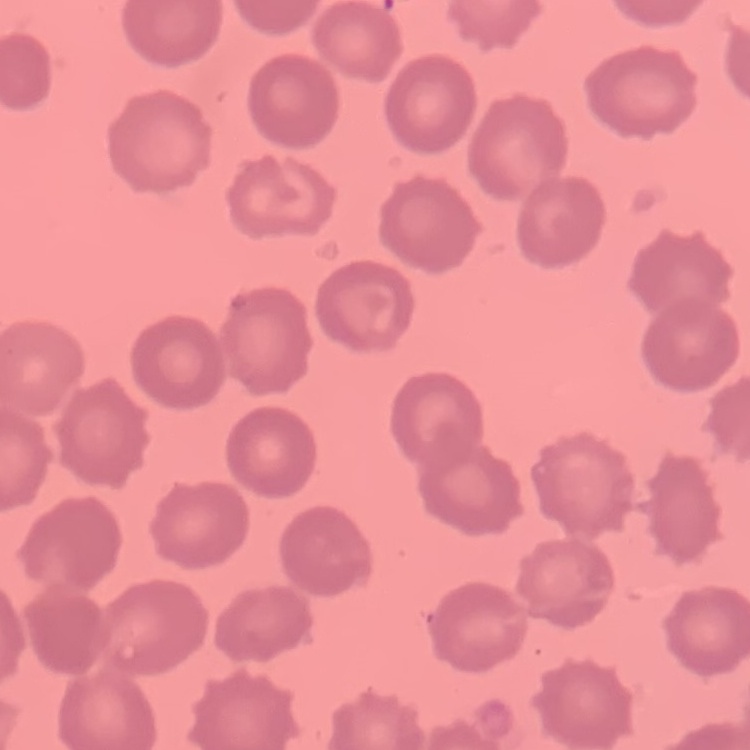

The red blood cells show no rouleaux formation. Square crop of a larger photomicrograph. Field's or Giemsa stain. Thin peripheral smear.